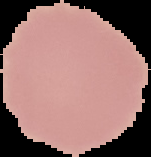
malaria_status: uninfected
preparation: thin blood smear
image_type: segmented cell region on a black background
image_size: 151×157 pixels